Name the cell type shown.
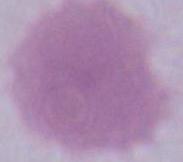
This is an erythrocyte.

1000x magnification. Photomicrograph.